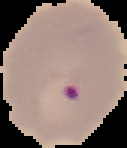 Image is 127×148 pixels. From a thin blood smear. Malaria status: parasitized. Segmented cell region on a black background.